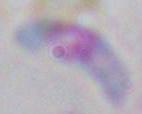 Toxoplasma gondii is shown. Micrograph. 1000x magnification.